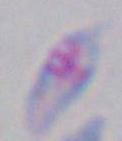
identification = Toxoplasma gondii
modality = photomicrograph
magnification = 1000x